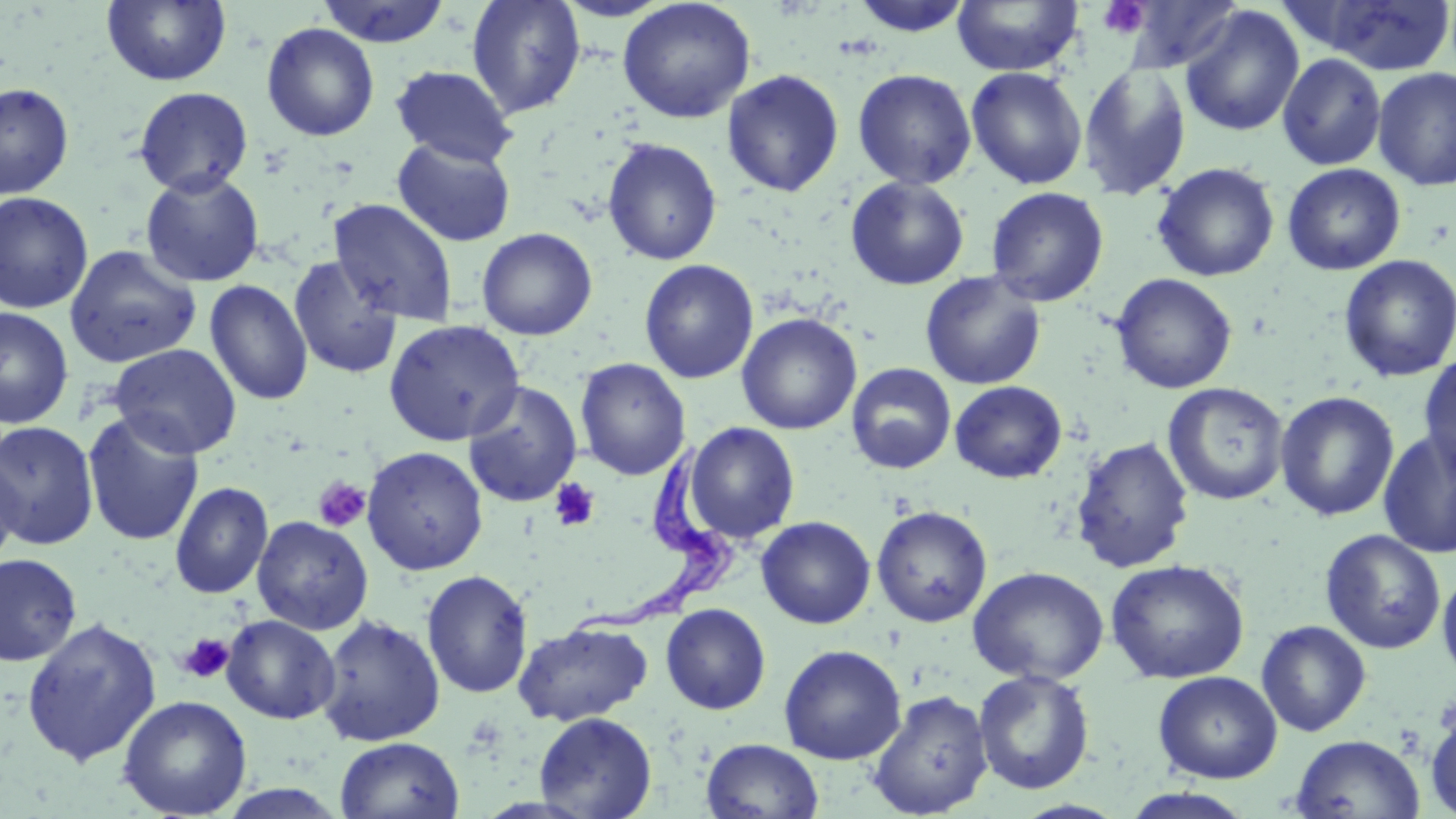

Approximate bounding boxes as [x1, y1, x2, y2] in pixels. Trypanosoma brucei locations: [574, 439, 743, 636]. Platelet locations: [1098, 1, 1149, 39], [313, 476, 371, 532], [549, 478, 601, 532], [177, 633, 235, 684]. Uninfected red blood cell locations: [102, 0, 231, 86], [315, 0, 452, 48], [466, 0, 586, 119], [553, 0, 676, 22], [617, 0, 756, 123], [848, 0, 974, 37], [951, 0, 1082, 77], [1120, 0, 1242, 73], [1308, 0, 1456, 75], [1180, 6, 1305, 137], [260, 22, 380, 142], [1277, 53, 1387, 171], [1077, 63, 1192, 202], [390, 65, 517, 167], [965, 66, 1087, 190], [1372, 67, 1456, 191], [852, 68, 977, 190], [721, 69, 844, 197], [0, 82, 75, 199], [133, 86, 254, 196], [390, 136, 517, 247], [602, 138, 723, 266], [1151, 162, 1280, 281], [1282, 163, 1406, 275], [139, 169, 265, 287], [845, 175, 970, 290], [986, 187, 1109, 307], [0, 190, 94, 314], [329, 198, 459, 327], [476, 227, 597, 340], [63, 244, 202, 369], [1337, 254, 1456, 383], [288, 255, 403, 380], [639, 259, 759, 384], [920, 271, 1047, 391], [1111, 273, 1237, 394], [204, 279, 313, 406], [0, 306, 74, 429], [736, 312, 861, 435], [383, 319, 525, 445], [108, 343, 242, 459], [1417, 353, 1456, 482], [574, 357, 691, 480], [846, 363, 957, 474], [462, 381, 583, 508], [950, 381, 1067, 484], [1162, 382, 1289, 506], [1274, 390, 1399, 522], [82, 411, 205, 547], [0, 420, 100, 549], [683, 422, 800, 544], [1377, 428, 1456, 559], [1070, 436, 1195, 574], [361, 446, 488, 576], [0, 449, 22, 573], [169, 481, 273, 599], [871, 505, 993, 628], [251, 515, 373, 635], [756, 516, 876, 629], [1319, 529, 1446, 654], [0, 553, 82, 667], [1105, 559, 1249, 684], [967, 565, 1109, 685], [1437, 568, 1456, 686], [421, 569, 534, 699], [660, 603, 771, 714], [315, 614, 446, 747], [221, 615, 340, 724], [21, 616, 161, 768], [1256, 620, 1371, 737], [513, 622, 653, 727], [778, 644, 907, 764], [973, 668, 1095, 796], [1153, 670, 1283, 783], [867, 690, 993, 818], [117, 695, 252, 818], [1424, 701, 1456, 819], [534, 711, 657, 818], [1290, 734, 1425, 819], [334, 736, 465, 819], [701, 738, 824, 819], [1117, 788, 1258, 819]. Slide-level diagnosis: Trypanosoma brucei. Optical microscopy. Captured at 1000x magnification. Image is 1456×819 pixels. One field of a larger specimen. May-Grünwald-Giemsa-stained preparation. Thin blood smear.